Outline each blood parasite and name the species.
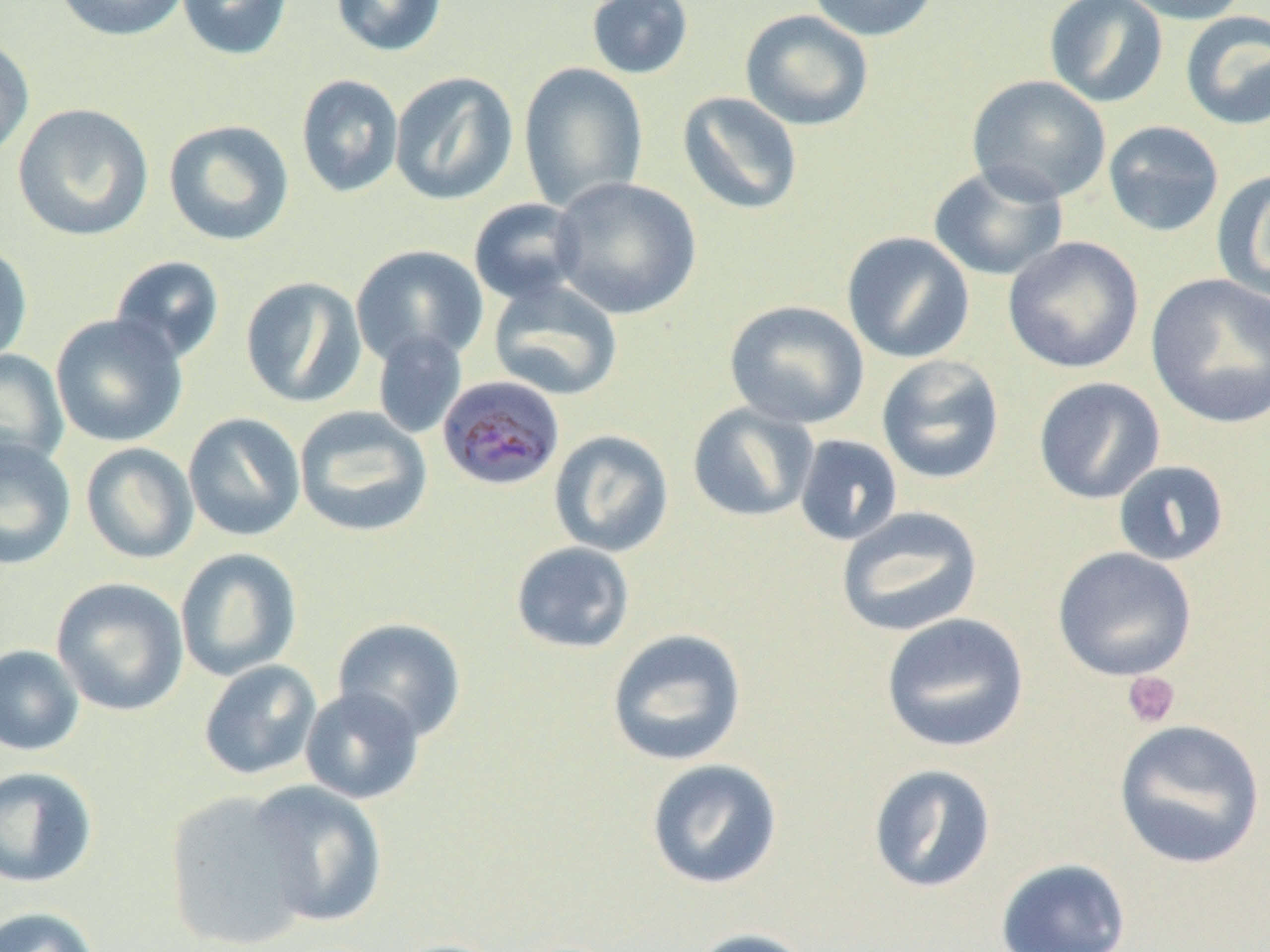
Approximate bounding boxes as named x1/y1/x2/y2 corners in pixels.
Plasmodium malariae-infected red blood cells: (x1=437, y1=376, x2=567, y2=492).
No Plasmodium falciparum, Plasmodium ovale, Plasmodium vivax, Babesia divergens, or Trypanosoma brucei observed.

Summary:
  - Platelet locations: (x1=1121, y1=670, x2=1181, y2=729)
  - Uninfected red blood cell locations: (x1=55, y1=0, x2=189, y2=42), (x1=176, y1=0, x2=294, y2=61), (x1=330, y1=0, x2=448, y2=58), (x1=585, y1=0, x2=695, y2=80), (x1=806, y1=0, x2=941, y2=42), (x1=1043, y1=0, x2=1169, y2=108), (x1=1114, y1=0, x2=1251, y2=25), (x1=739, y1=9, x2=874, y2=131), (x1=1180, y1=11, x2=1270, y2=131), (x1=0, y1=34, x2=34, y2=162), (x1=518, y1=63, x2=649, y2=213), (x1=389, y1=71, x2=519, y2=206), (x1=295, y1=75, x2=404, y2=199), (x1=967, y1=75, x2=1111, y2=205), (x1=677, y1=91, x2=803, y2=216), (x1=12, y1=103, x2=154, y2=241), (x1=163, y1=119, x2=295, y2=247), (x1=1102, y1=120, x2=1224, y2=238), (x1=927, y1=163, x2=1069, y2=282), (x1=1211, y1=171, x2=1270, y2=302), (x1=550, y1=176, x2=701, y2=320), (x1=468, y1=198, x2=587, y2=305), (x1=841, y1=231, x2=975, y2=364), (x1=1003, y1=236, x2=1145, y2=374), (x1=0, y1=242, x2=33, y2=365), (x1=350, y1=244, x2=488, y2=368), (x1=109, y1=255, x2=225, y2=365), (x1=1145, y1=273, x2=1270, y2=428), (x1=240, y1=276, x2=367, y2=408), (x1=488, y1=280, x2=624, y2=401), (x1=724, y1=300, x2=870, y2=430), (x1=50, y1=313, x2=188, y2=447), (x1=372, y1=330, x2=468, y2=440), (x1=0, y1=350, x2=69, y2=473), (x1=876, y1=355, x2=1005, y2=485), (x1=1032, y1=376, x2=1166, y2=505), (x1=687, y1=402, x2=819, y2=523), (x1=294, y1=406, x2=433, y2=538), (x1=183, y1=412, x2=305, y2=541), (x1=549, y1=429, x2=674, y2=557), (x1=793, y1=434, x2=903, y2=546), (x1=0, y1=436, x2=77, y2=571), (x1=81, y1=442, x2=199, y2=564), (x1=1112, y1=460, x2=1230, y2=566), (x1=835, y1=506, x2=984, y2=637), (x1=510, y1=541, x2=636, y2=654), (x1=1052, y1=546, x2=1197, y2=682), (x1=174, y1=547, x2=302, y2=682), (x1=51, y1=577, x2=190, y2=716), (x1=880, y1=612, x2=1030, y2=754), (x1=332, y1=617, x2=467, y2=743), (x1=606, y1=628, x2=747, y2=767), (x1=0, y1=644, x2=85, y2=756), (x1=198, y1=659, x2=322, y2=780), (x1=299, y1=686, x2=426, y2=804), (x1=1112, y1=718, x2=1266, y2=870), (x1=645, y1=758, x2=783, y2=890), (x1=868, y1=763, x2=997, y2=894), (x1=0, y1=766, x2=98, y2=889), (x1=246, y1=780, x2=389, y2=928), (x1=163, y1=790, x2=317, y2=951), (x1=995, y1=858, x2=1132, y2=952), (x1=0, y1=905, x2=102, y2=952), (x1=684, y1=927, x2=818, y2=952), (x1=381, y1=937, x2=512, y2=952)
  - Slide-level diagnosis: Plasmodium malariae
  - Image size: 1270×952 pixels
  - Field of view: one of a larger specimen
  - Preparation: thin blood smear
  - Magnification: 1000x
  - Modality: light microscopy